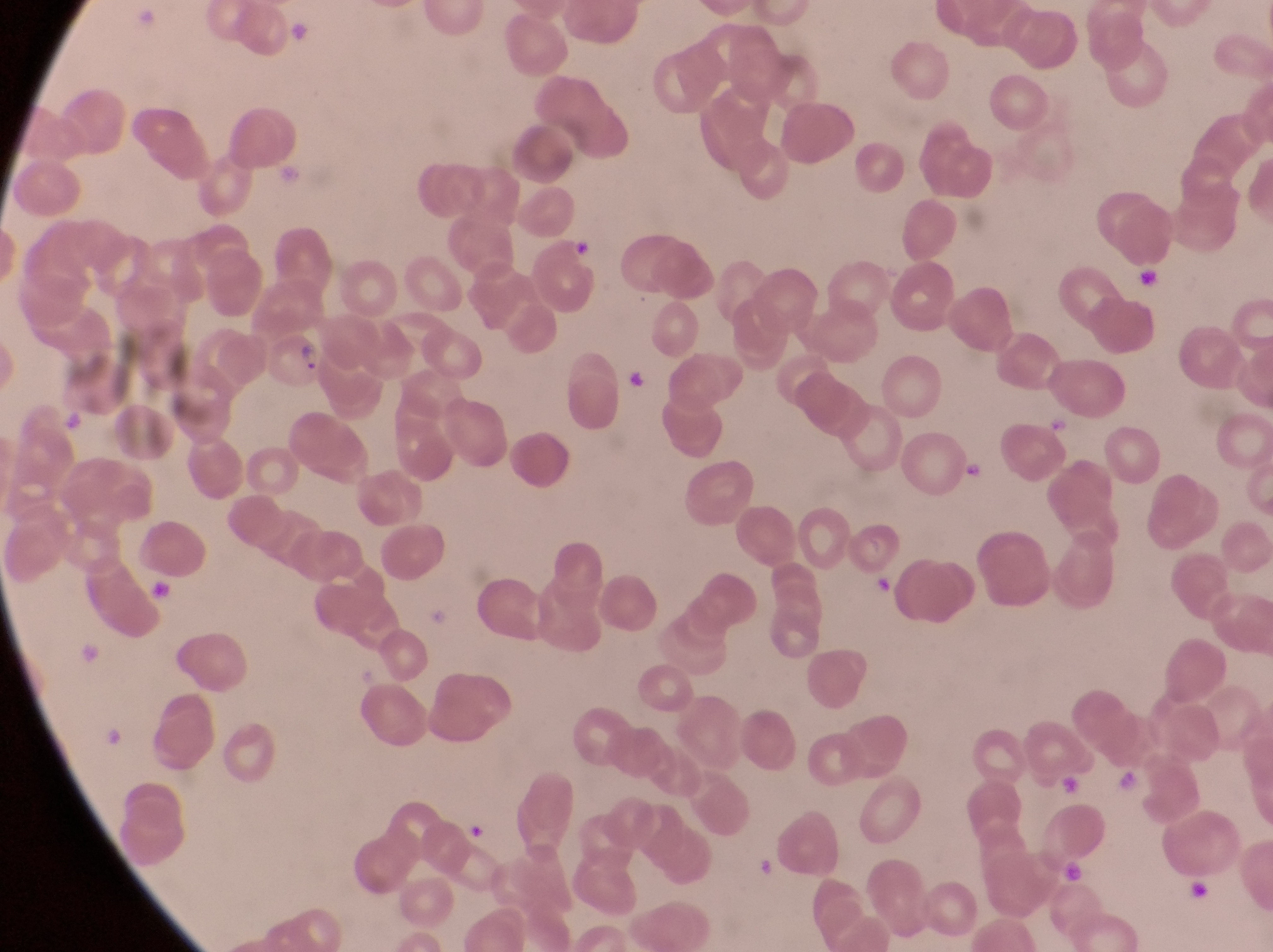
Approximate bounding boxes as (left, top, right, bottom) in pixels. Artifact (platelet-like body, stain precipitate, or debris) locations: (569, 239, 599, 264), (1134, 259, 1164, 296), (630, 367, 650, 393), (868, 569, 905, 597), (147, 574, 174, 602), (76, 638, 100, 665), (1117, 771, 1143, 797). Parasitised red blood cell locations: (265, 332, 323, 397). Trophozoite locations: (964, 457, 989, 485). Single field of view. Sample from Uganda. Image is 1273×952 pixels. Magnification of 1000x. Captured by a smartphone held over the eyepiece of an Olympus CX-23 microscope. Thin blood film.